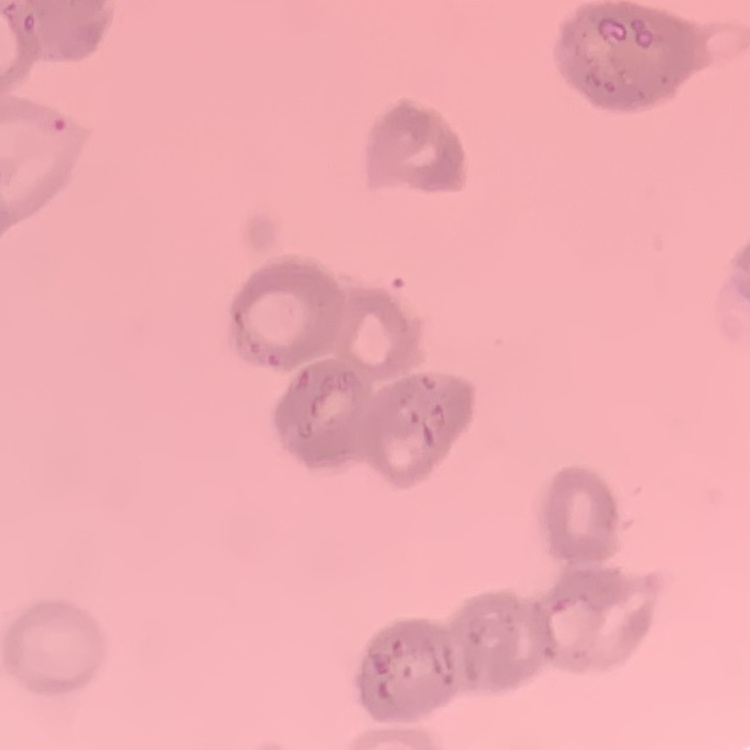
Summary:
  - Erythrocyte morphology: rouleaux formation
  - Image type: square crop of a larger photomicrograph
  - Preparation: thin blood film
  - Stain: Field's or Giemsa